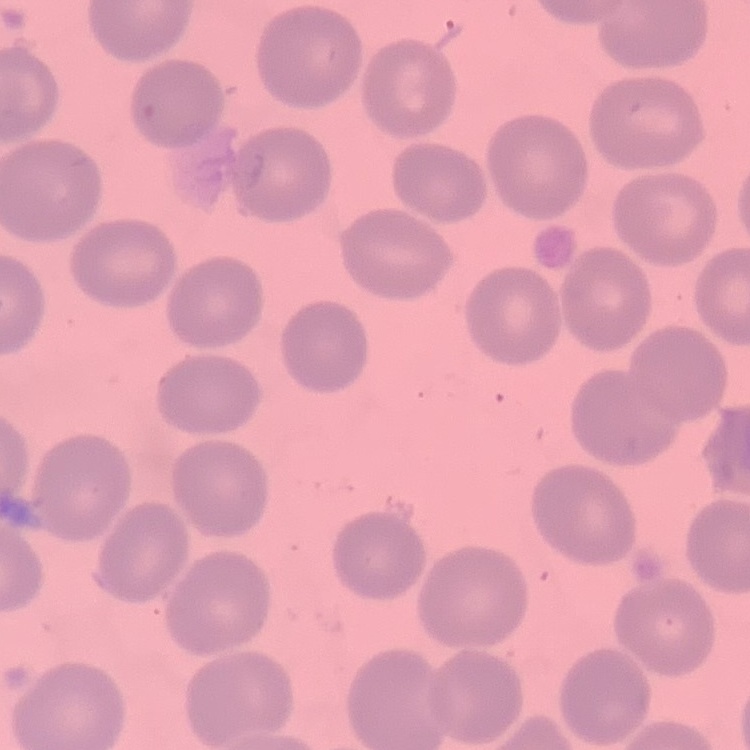
Summary:
  - Red blood cell morphology: no rouleaux formation
  - Image type: square crop of a larger photomicrograph
  - Stain: Field's or Giemsa
  - Preparation: thin blood film